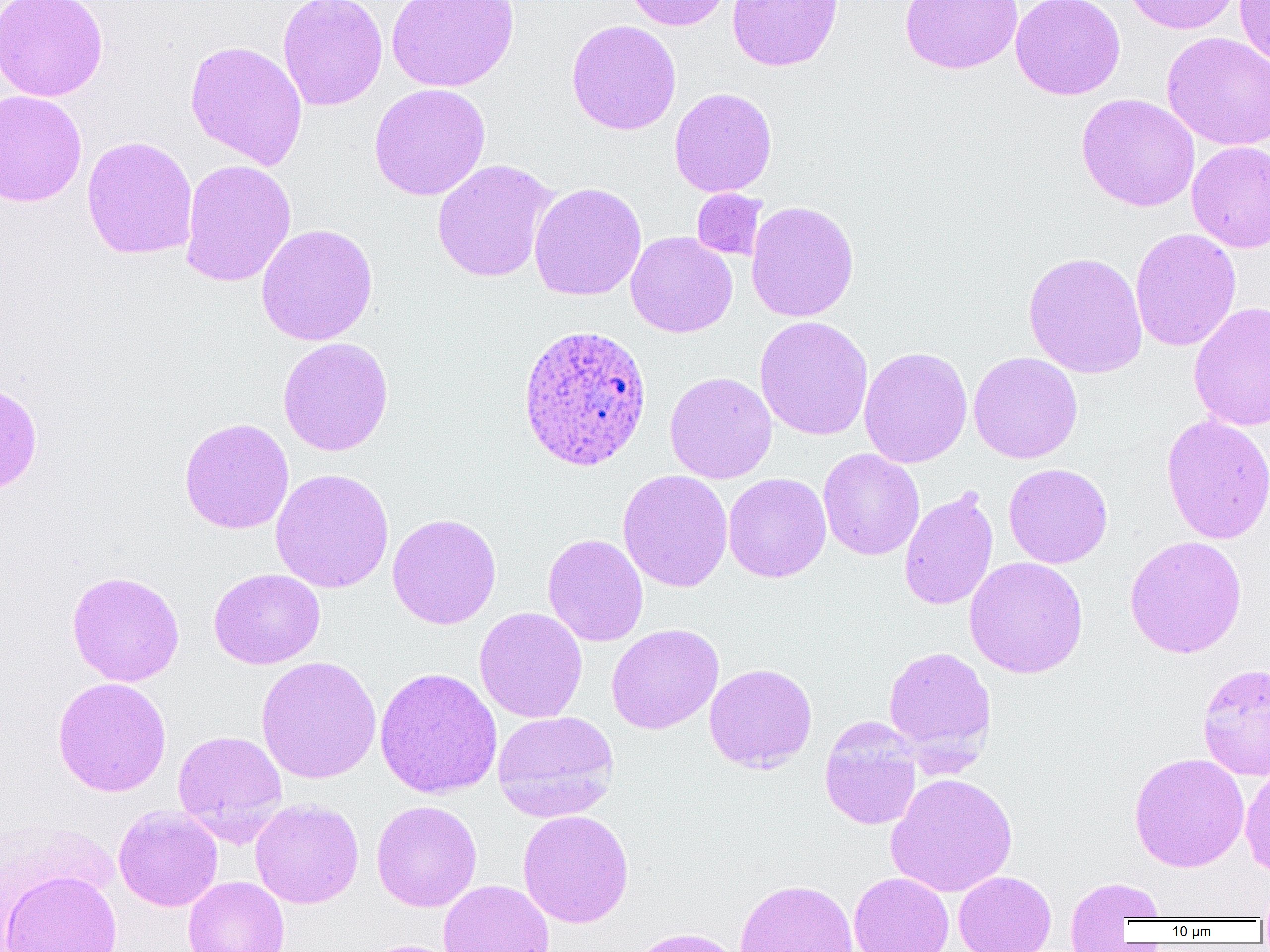

slide-level diagnosis = Plasmodium ovale
image size = 1270×952 pixels
Plasmodium ovale-infected red blood cell locations = approximate bounding boxes as (x1,y1)-(x2,y2) corner pairs in pixels: (517,322)-(654,472)
modality = optical microscopy
field of view = one of a larger specimen
magnification = 1000x
uninfected red blood cell locations = approximate bounding boxes as (x1,y1)-(x2,y2) corner pairs in pixels: (0,0)-(109,101), (277,0)-(388,111), (386,0)-(519,92), (624,0)-(732,30), (726,0)-(844,71), (899,0)-(1024,75), (1010,0)-(1125,100), (1122,0)-(1242,34), (1234,0)-(1270,67), (566,19)-(681,135), (1162,31)-(1270,151), (185,39)-(308,170), (369,83)-(490,201), (669,87)-(777,198), (0,89)-(87,208), (1076,93)-(1200,212), (81,136)-(198,260), (1186,141)-(1270,254), (179,159)-(297,287), (431,159)-(559,283), (529,182)-(647,300), (692,189)-(768,261), (745,200)-(860,322), (255,223)-(378,345), (1130,227)-(1242,352), (626,231)-(737,338), (1022,251)-(1147,378), (1188,302)-(1270,432), (754,315)-(873,441), (277,336)-(394,456), (859,345)-(973,468), (969,351)-(1082,464), (664,371)-(777,484), (0,382)-(43,495), (1160,414)-(1270,545), (179,417)-(294,533), (818,449)-(924,561), (1003,463)-(1113,568), (270,468)-(394,593), (617,470)-(733,592), (723,473)-(831,582), (898,488)-(998,611), (387,513)-(502,629), (542,533)-(648,646), (1124,535)-(1247,659), (964,556)-(1089,679), (209,568)-(326,669), (66,570)-(185,687), (474,607)-(587,723), (606,623)-(724,734), (882,645)-(997,766), (256,656)-(381,784), (704,663)-(817,773), (1197,663)-(1270,781), (375,667)-(502,800), (52,676)-(172,797), (492,710)-(620,822), (819,717)-(922,830), (172,729)-(287,842), (1129,752)-(1249,872), (1240,764)-(1270,879), (886,772)-(1018,897), (250,799)-(364,909), (371,800)-(482,912), (113,806)-(223,911), (517,809)-(634,928), (0,869)-(123,952), (953,871)-(1056,952), (849,872)-(954,952), (1064,875)-(1166,943), (183,876)-(289,952), (733,878)-(859,952), (438,880)-(554,952), (1255,882)-(1270,923), (623,926)-(747,952), (360,939)-(463,952)
preparation = thin blood film